Identify the parasite.
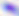

Toxoplasma gondii.

Photomicrograph. Captured at 400x magnification.